Outline each blood parasite and name the species.
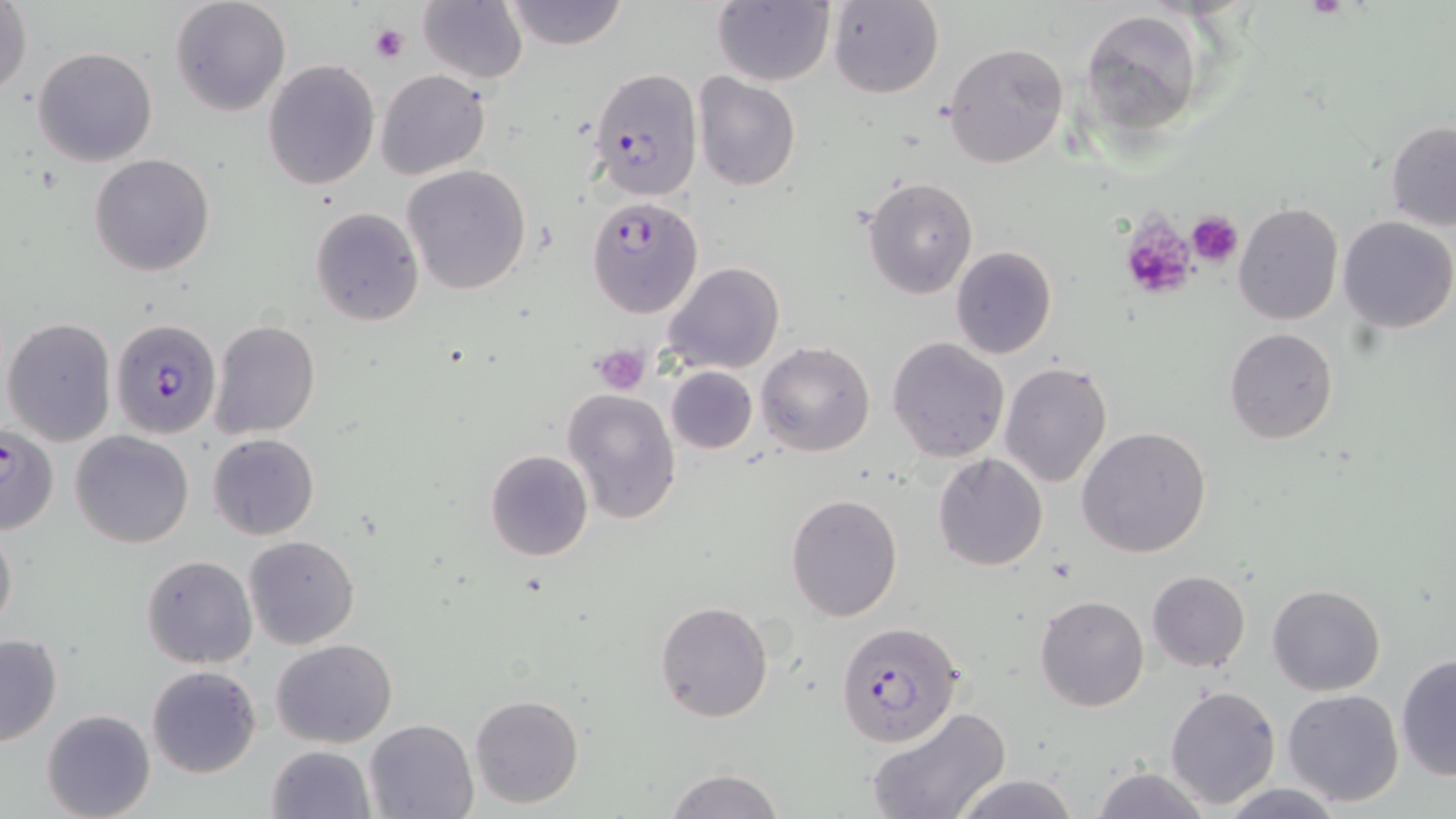
Approximate bounding boxes as named x1/y1/x2/y2 corners in pixels.
Plasmodium falciparum-infected red blood cells: (x1=588, y1=67, x2=702, y2=202), (x1=587, y1=196, x2=704, y2=318), (x1=111, y1=318, x2=221, y2=439), (x1=0, y1=421, x2=60, y2=532), (x1=836, y1=620, x2=965, y2=746).
No Plasmodium ovale, Plasmodium malariae, Plasmodium vivax, Babesia divergens, or Trypanosoma brucei observed.

Summary:
  - Uninfected red blood cell locations: (x1=170, y1=0, x2=291, y2=116), (x1=502, y1=0, x2=628, y2=49), (x1=712, y1=0, x2=835, y2=86), (x1=828, y1=0, x2=943, y2=99), (x1=418, y1=1, x2=528, y2=85), (x1=1, y1=2, x2=32, y2=100), (x1=1078, y1=9, x2=1205, y2=135), (x1=943, y1=41, x2=1069, y2=171), (x1=33, y1=46, x2=159, y2=168), (x1=262, y1=61, x2=380, y2=190), (x1=376, y1=70, x2=490, y2=179), (x1=693, y1=73, x2=802, y2=191), (x1=1385, y1=121, x2=1456, y2=231), (x1=89, y1=154, x2=215, y2=276), (x1=402, y1=165, x2=532, y2=296), (x1=861, y1=176, x2=977, y2=297), (x1=1233, y1=202, x2=1342, y2=325), (x1=310, y1=207, x2=424, y2=325), (x1=1337, y1=215, x2=1455, y2=332), (x1=950, y1=246, x2=1057, y2=359), (x1=663, y1=262, x2=785, y2=375), (x1=3, y1=317, x2=117, y2=447), (x1=210, y1=319, x2=320, y2=438), (x1=1223, y1=327, x2=1339, y2=444), (x1=887, y1=336, x2=1010, y2=463), (x1=756, y1=341, x2=874, y2=457), (x1=998, y1=361, x2=1114, y2=488), (x1=666, y1=365, x2=758, y2=453), (x1=562, y1=387, x2=682, y2=524), (x1=1077, y1=425, x2=1211, y2=558), (x1=71, y1=429, x2=194, y2=548), (x1=208, y1=433, x2=320, y2=541), (x1=485, y1=449, x2=594, y2=561), (x1=933, y1=453, x2=1048, y2=571), (x1=786, y1=493, x2=903, y2=621), (x1=0, y1=518, x2=17, y2=637), (x1=243, y1=535, x2=360, y2=649), (x1=141, y1=555, x2=258, y2=670), (x1=1146, y1=571, x2=1250, y2=672), (x1=1267, y1=583, x2=1385, y2=695), (x1=1035, y1=594, x2=1149, y2=712), (x1=654, y1=599, x2=774, y2=723), (x1=0, y1=632, x2=63, y2=749), (x1=272, y1=638, x2=398, y2=747), (x1=1395, y1=654, x2=1455, y2=780), (x1=146, y1=665, x2=262, y2=779), (x1=1165, y1=684, x2=1282, y2=809), (x1=1280, y1=689, x2=1404, y2=807), (x1=468, y1=694, x2=584, y2=809), (x1=865, y1=706, x2=1010, y2=819), (x1=41, y1=708, x2=155, y2=819), (x1=364, y1=718, x2=479, y2=819), (x1=268, y1=743, x2=375, y2=818), (x1=1089, y1=765, x2=1207, y2=819), (x1=667, y1=769, x2=784, y2=819), (x1=954, y1=775, x2=1079, y2=819), (x1=1218, y1=782, x2=1346, y2=817)
  - Platelet locations: (x1=369, y1=23, x2=407, y2=64), (x1=1186, y1=211, x2=1243, y2=269), (x1=1118, y1=216, x2=1197, y2=301), (x1=592, y1=343, x2=650, y2=396)
  - Slide-level diagnosis: Plasmodium falciparum
  - Preparation: thin blood smear
  - Magnification: 1000x
  - Image size: 1456×819 pixels
  - Stain: May-Grünwald-Giemsa
  - Field of view: one of a larger specimen
  - Modality: light microscopy